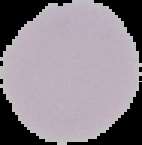

Summary:
  - Result: no Plasmodium parasites detected
  - Image size: 142×145 pixels
  - Image type: segmented cell region with the area outside set to black
  - Preparation: thin blood film